Comment on the morphology of the erythrocytes.
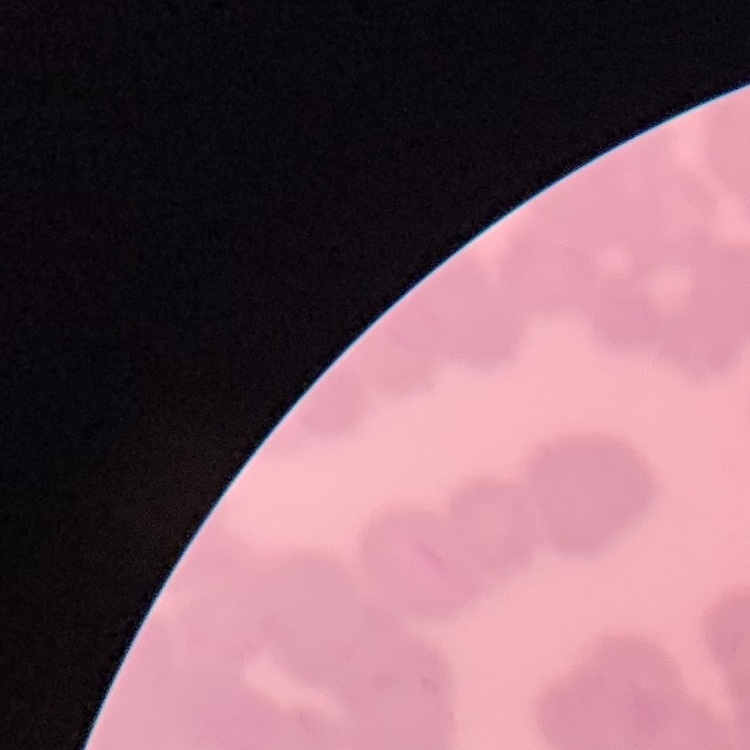
Rouleaux formation.

One tile cut from a larger photomicrograph. Field's or Giemsa stain. Thin blood film.